Describe the morphology of the erythrocytes.
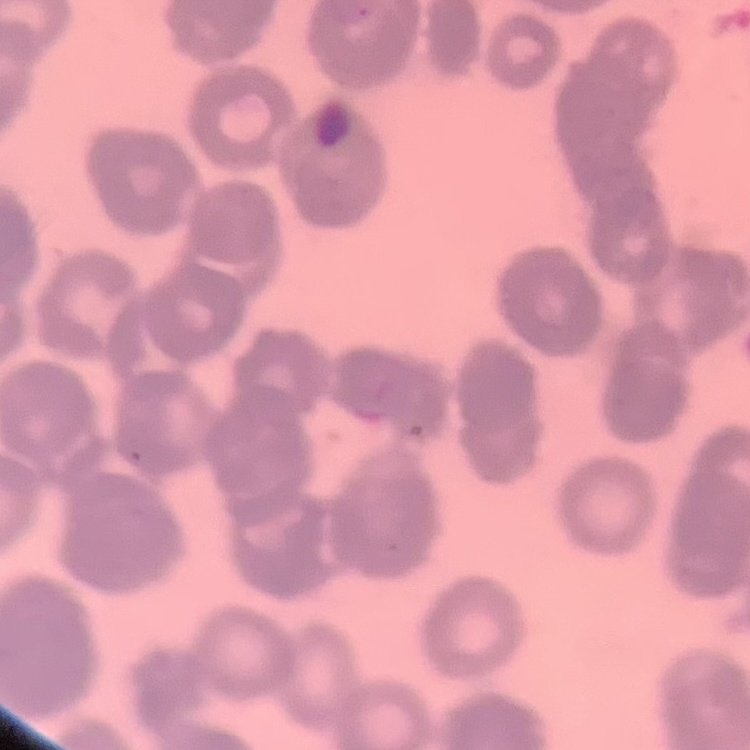
They show rouleaux formation.

Stained with either Field's or Giemsa. Thin peripheral smear. Square crop of a larger photomicrograph.